Name the blood parasite species.
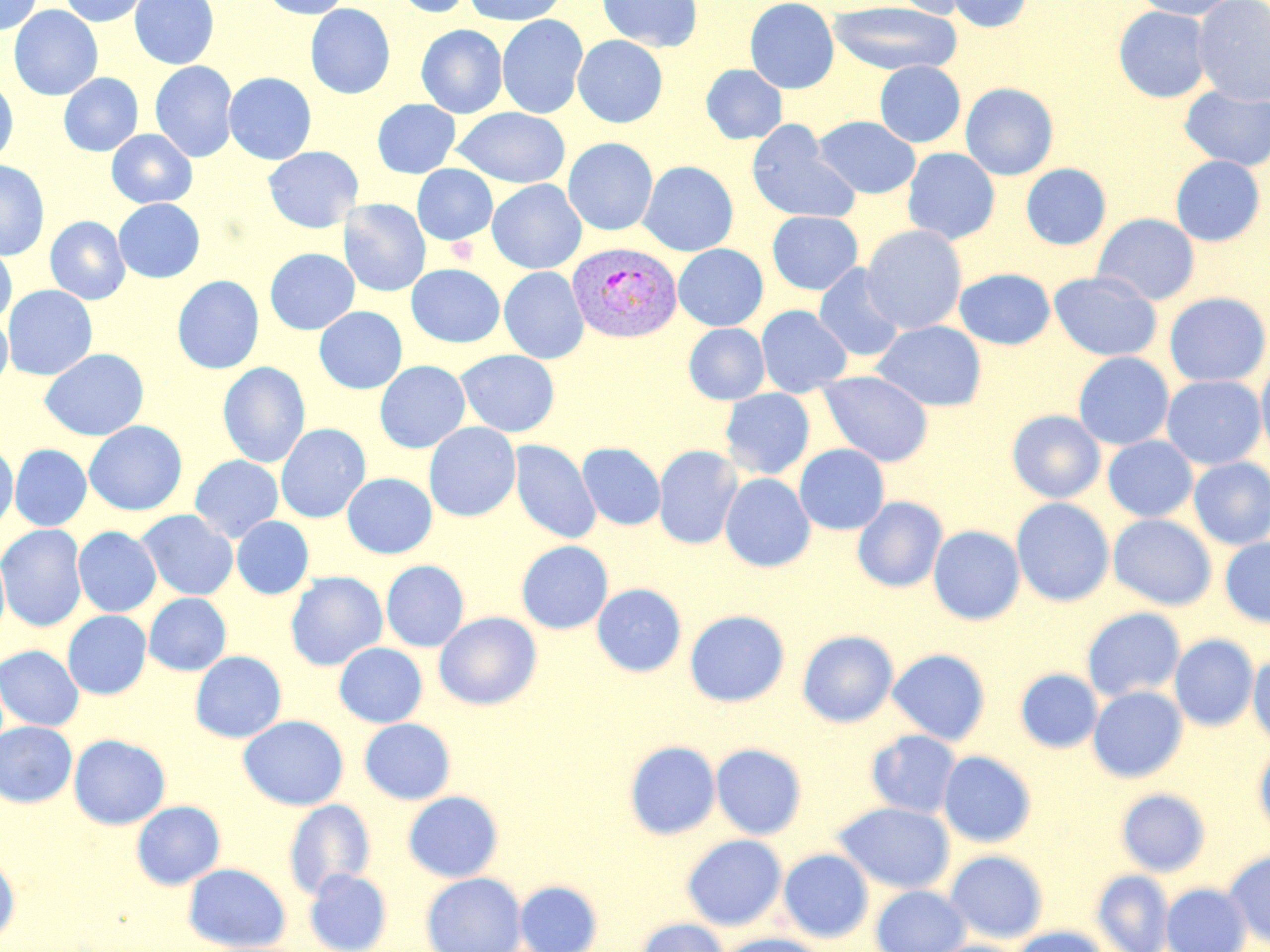

Plasmodium vivax.

Approximate bounding boxes as named x1/y1/x2/y2 corners in pixels. Plasmodium vivax-infected red blood cell locations: (x1=567, y1=241, x2=682, y2=343). Platelet locations: (x1=445, y1=235, x2=477, y2=265). Uninfected red blood cell locations: (x1=1, y1=0, x2=43, y2=36), (x1=58, y1=0, x2=151, y2=27), (x1=129, y1=0, x2=219, y2=69), (x1=260, y1=0, x2=353, y2=19), (x1=391, y1=0, x2=476, y2=18), (x1=463, y1=0, x2=568, y2=26), (x1=597, y1=0, x2=702, y2=52), (x1=744, y1=0, x2=840, y2=93), (x1=891, y1=0, x2=971, y2=19), (x1=947, y1=0, x2=1032, y2=33), (x1=1133, y1=0, x2=1239, y2=20), (x1=1192, y1=0, x2=1270, y2=105), (x1=827, y1=2, x2=962, y2=76), (x1=305, y1=3, x2=395, y2=99), (x1=9, y1=4, x2=103, y2=100), (x1=1113, y1=6, x2=1212, y2=102), (x1=497, y1=14, x2=589, y2=119), (x1=416, y1=24, x2=507, y2=118), (x1=572, y1=35, x2=668, y2=128), (x1=150, y1=61, x2=238, y2=163), (x1=874, y1=61, x2=965, y2=147), (x1=700, y1=64, x2=787, y2=144), (x1=224, y1=72, x2=316, y2=165), (x1=59, y1=73, x2=143, y2=156), (x1=0, y1=77, x2=18, y2=166), (x1=960, y1=82, x2=1059, y2=180), (x1=1179, y1=85, x2=1270, y2=171), (x1=372, y1=99, x2=460, y2=178), (x1=452, y1=107, x2=570, y2=188), (x1=814, y1=116, x2=920, y2=199), (x1=746, y1=120, x2=860, y2=225), (x1=106, y1=129, x2=197, y2=208), (x1=563, y1=137, x2=658, y2=235), (x1=263, y1=146, x2=363, y2=232), (x1=902, y1=148, x2=1000, y2=245), (x1=1170, y1=155, x2=1265, y2=246), (x1=0, y1=160, x2=50, y2=261), (x1=638, y1=160, x2=739, y2=256), (x1=1021, y1=163, x2=1111, y2=250), (x1=412, y1=164, x2=498, y2=245), (x1=487, y1=179, x2=586, y2=274), (x1=113, y1=198, x2=204, y2=283), (x1=339, y1=198, x2=431, y2=297), (x1=766, y1=211, x2=863, y2=295), (x1=1092, y1=213, x2=1200, y2=305), (x1=45, y1=216, x2=130, y2=304), (x1=861, y1=225, x2=967, y2=334), (x1=0, y1=243, x2=17, y2=326), (x1=673, y1=244, x2=768, y2=331), (x1=265, y1=248, x2=359, y2=335), (x1=406, y1=263, x2=505, y2=347), (x1=813, y1=263, x2=906, y2=362), (x1=499, y1=266, x2=589, y2=364), (x1=954, y1=268, x2=1055, y2=350), (x1=1049, y1=271, x2=1162, y2=361), (x1=172, y1=275, x2=264, y2=374), (x1=3, y1=284, x2=97, y2=380), (x1=1164, y1=292, x2=1269, y2=387), (x1=756, y1=305, x2=852, y2=397), (x1=314, y1=306, x2=407, y2=393), (x1=0, y1=312, x2=13, y2=390), (x1=872, y1=320, x2=987, y2=411), (x1=684, y1=323, x2=769, y2=404), (x1=40, y1=348, x2=149, y2=441), (x1=456, y1=349, x2=560, y2=437), (x1=1073, y1=351, x2=1174, y2=450), (x1=1256, y1=356, x2=1270, y2=464), (x1=375, y1=360, x2=470, y2=453), (x1=217, y1=362, x2=310, y2=468), (x1=817, y1=370, x2=934, y2=467), (x1=1161, y1=375, x2=1266, y2=469), (x1=720, y1=388, x2=815, y2=479), (x1=1007, y1=410, x2=1105, y2=503), (x1=84, y1=421, x2=187, y2=515), (x1=423, y1=422, x2=521, y2=522), (x1=275, y1=423, x2=370, y2=522), (x1=1103, y1=436, x2=1198, y2=522), (x1=510, y1=440, x2=601, y2=544), (x1=577, y1=442, x2=665, y2=530), (x1=0, y1=443, x2=18, y2=532), (x1=794, y1=443, x2=889, y2=535), (x1=9, y1=444, x2=92, y2=531), (x1=653, y1=445, x2=742, y2=549), (x1=190, y1=455, x2=283, y2=542), (x1=1188, y1=457, x2=1270, y2=549), (x1=342, y1=472, x2=437, y2=558), (x1=720, y1=473, x2=815, y2=572), (x1=852, y1=496, x2=947, y2=592), (x1=1011, y1=497, x2=1114, y2=607), (x1=136, y1=509, x2=238, y2=600), (x1=1108, y1=514, x2=1217, y2=610), (x1=231, y1=516, x2=314, y2=599), (x1=0, y1=524, x2=88, y2=632), (x1=928, y1=525, x2=1025, y2=625), (x1=73, y1=526, x2=161, y2=617), (x1=1220, y1=538, x2=1270, y2=628), (x1=516, y1=540, x2=613, y2=634), (x1=0, y1=547, x2=10, y2=643), (x1=381, y1=560, x2=469, y2=651), (x1=285, y1=571, x2=387, y2=671), (x1=592, y1=583, x2=686, y2=677), (x1=144, y1=593, x2=231, y2=676), (x1=1081, y1=607, x2=1186, y2=702), (x1=684, y1=609, x2=790, y2=707), (x1=62, y1=610, x2=151, y2=699), (x1=433, y1=611, x2=542, y2=710), (x1=797, y1=630, x2=898, y2=727), (x1=1170, y1=634, x2=1259, y2=731), (x1=334, y1=643, x2=427, y2=727), (x1=0, y1=645, x2=84, y2=731), (x1=887, y1=648, x2=991, y2=745), (x1=190, y1=650, x2=287, y2=743), (x1=1248, y1=653, x2=1270, y2=748), (x1=1015, y1=668, x2=1103, y2=753), (x1=1088, y1=686, x2=1187, y2=782), (x1=238, y1=715, x2=348, y2=810), (x1=359, y1=718, x2=456, y2=804), (x1=0, y1=721, x2=77, y2=807), (x1=866, y1=729, x2=961, y2=818), (x1=69, y1=734, x2=170, y2=830), (x1=624, y1=741, x2=720, y2=840), (x1=1254, y1=742, x2=1270, y2=841), (x1=711, y1=743, x2=807, y2=839), (x1=939, y1=750, x2=1037, y2=848), (x1=1116, y1=788, x2=1210, y2=876), (x1=403, y1=791, x2=503, y2=882), (x1=284, y1=799, x2=375, y2=898), (x1=131, y1=800, x2=225, y2=889), (x1=834, y1=802, x2=955, y2=893), (x1=682, y1=834, x2=787, y2=930), (x1=1224, y1=848, x2=1270, y2=949), (x1=779, y1=849, x2=873, y2=943), (x1=944, y1=850, x2=1048, y2=943), (x1=0, y1=853, x2=20, y2=943), (x1=182, y1=862, x2=291, y2=951), (x1=304, y1=868, x2=392, y2=952), (x1=1091, y1=869, x2=1174, y2=952), (x1=421, y1=872, x2=526, y2=952), (x1=514, y1=880, x2=603, y2=952), (x1=1161, y1=883, x2=1251, y2=952), (x1=871, y1=884, x2=970, y2=952), (x1=634, y1=918, x2=730, y2=952), (x1=1012, y1=926, x2=1111, y2=952), (x1=716, y1=933, x2=828, y2=952), (x1=924, y1=939, x2=1027, y2=952). One field of a larger specimen. Optical microscopy. 1000x magnification. Image is 1270×952 pixels. May-Grünwald-Giemsa-stained preparation. Thin blood film.